State which parasite is depicted.
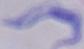

A trypanosome.

{
  "magnification": "1000x",
  "modality": "micrograph"
}